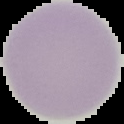
image type = cell region segmented out of the field of view; surrounding area masked to black
malaria status = uninfected
preparation = thin blood smear
image size = 124×124 pixels